Give the extent of all uninfected red blood cells.
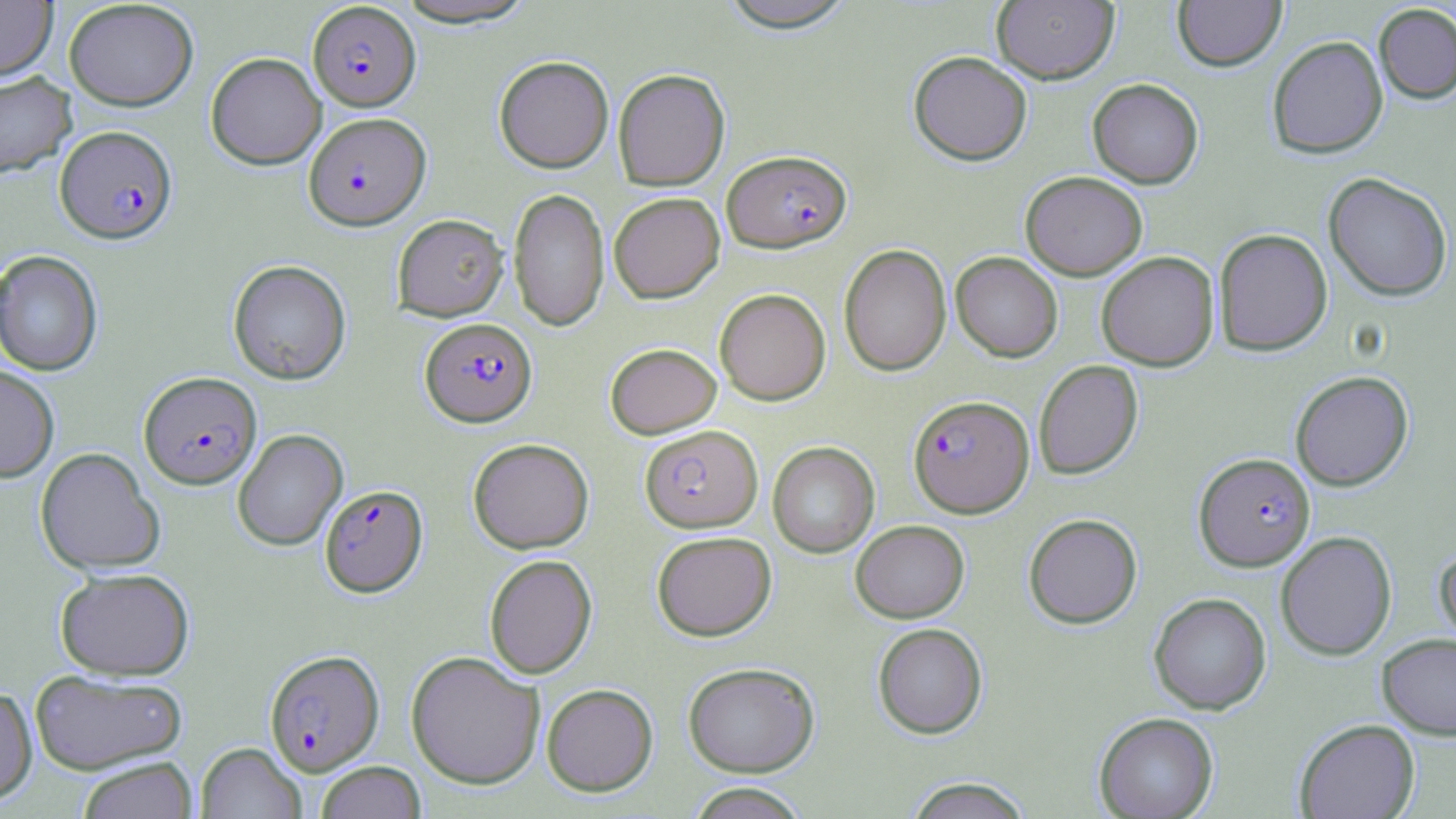
Approximate bounding boxes as (x1, y1, x2, y2) in pixels.
Uninfected red blood cells: (392, 0, 539, 28), (715, 0, 860, 31), (992, 0, 1119, 84), (1173, 0, 1287, 71), (0, 1, 57, 80), (63, 1, 199, 111), (1373, 3, 1456, 104), (1267, 36, 1388, 158), (908, 51, 1032, 165), (205, 52, 326, 170), (494, 55, 614, 173), (612, 68, 730, 190), (0, 72, 77, 179), (1087, 78, 1203, 188), (1020, 171, 1148, 280), (1323, 172, 1453, 302), (508, 187, 609, 332), (608, 192, 725, 303), (392, 214, 509, 321), (1213, 228, 1333, 356), (839, 244, 951, 377), (0, 250, 103, 376), (1096, 251, 1219, 371), (950, 252, 1063, 362), (228, 259, 351, 385), (714, 288, 831, 405), (605, 343, 721, 439), (1034, 360, 1143, 479), (0, 365, 60, 483), (1290, 371, 1414, 491), (232, 429, 348, 551), (468, 438, 594, 554), (767, 441, 879, 558), (35, 447, 165, 574), (1023, 513, 1142, 628), (850, 519, 969, 623), (651, 530, 776, 641), (1275, 531, 1397, 660), (1434, 546, 1456, 651), (484, 554, 597, 679), (55, 567, 194, 680), (1148, 592, 1272, 714), (872, 623, 988, 739), (1377, 633, 1456, 739), (406, 651, 545, 789), (682, 662, 820, 777), (29, 669, 188, 775), (541, 683, 658, 796), (0, 685, 38, 806), (1093, 712, 1219, 818), (1294, 718, 1420, 819), (196, 742, 307, 818), (77, 757, 198, 819), (315, 760, 427, 819), (903, 777, 1034, 819), (685, 782, 811, 819).

{
  "slide_level_diagnosis": "Plasmodium falciparum",
  "stain": "May-Grünwald-Giemsa",
  "modality": "optical microscopy",
  "field_of_view": "single",
  "magnification": "1000x",
  "preparation": "thin blood film",
  "image_size": "1456×819 pixels",
  "plasmodium_falciparum_infected_red_blood_cell_locations": "approximate bounding boxes as (x1, y1, x2, y2) in pixels: (307, 2, 421, 111), (304, 112, 430, 230), (55, 125, 177, 244), (722, 149, 852, 252), (420, 317, 537, 426), (138, 371, 261, 489), (908, 395, 1035, 517), (639, 424, 763, 532), (1194, 453, 1315, 571), (319, 484, 428, 597), (264, 649, 384, 775)"
}